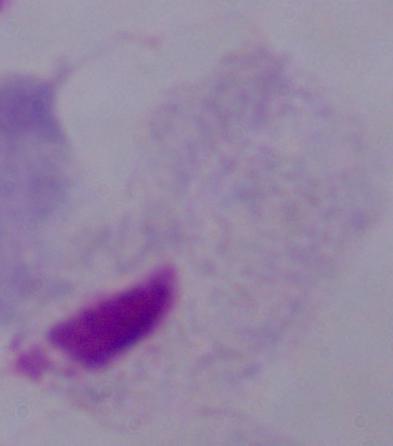
{
  "identification": "trichomonad",
  "modality": "photomicrograph",
  "magnification": "1000x"
}